State which parasite is depicted.
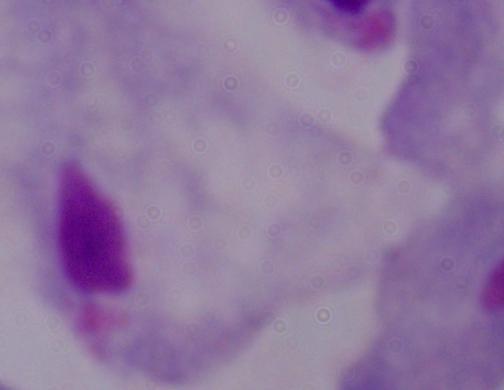
A trichomonad.

Captured at 1000x magnification. Micrograph.